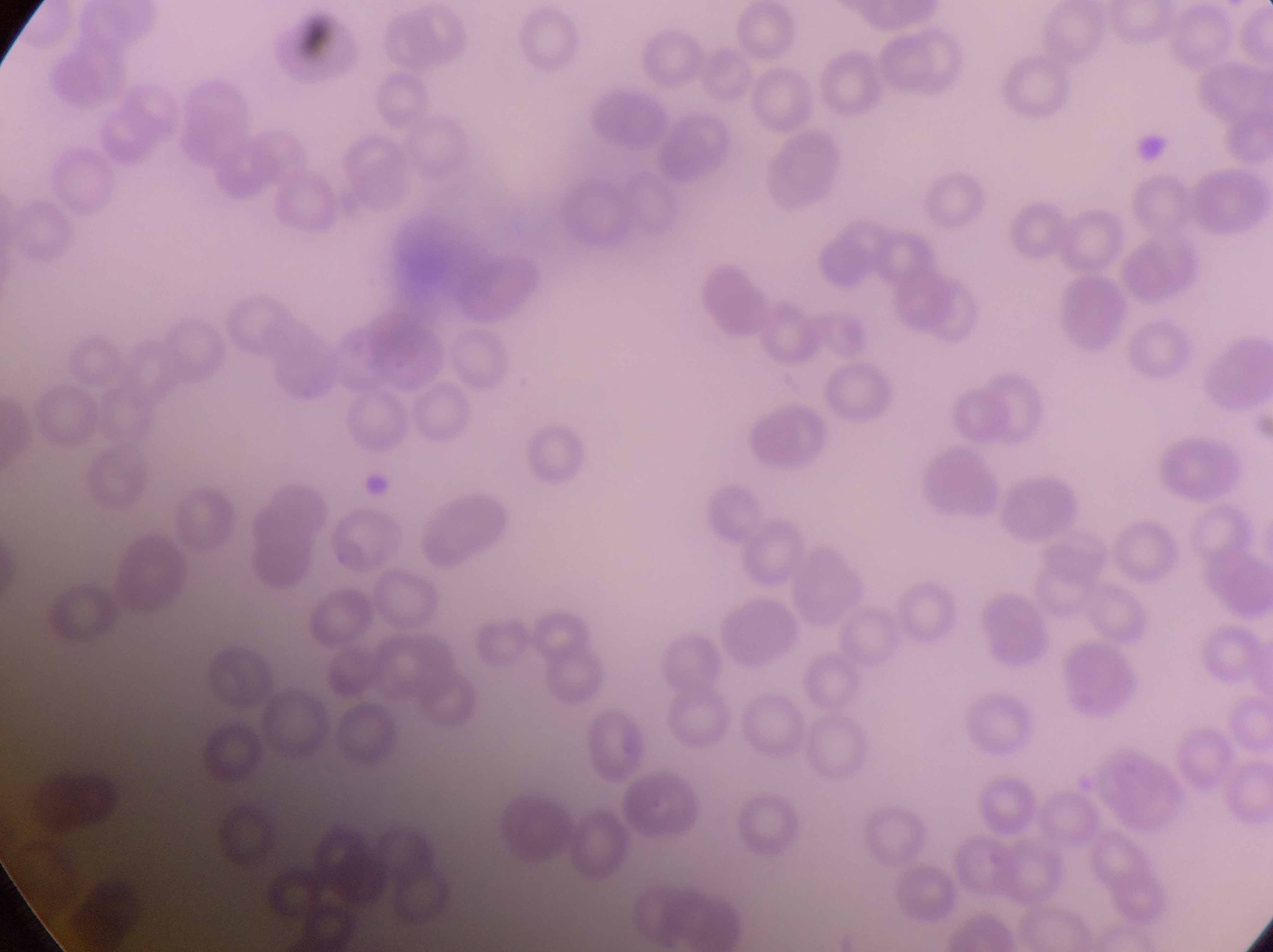
Approximate bounding boxes as left top right bottom in pixels.
Summary:
  - Artifact (platelet-like body, stain precipitate, or debris) locations: 1130 130 1170 169
  - Parasitised red blood cell locations: 325 509 413 579
  - Preparation: thin blood smear
  - Field of view: single
  - Magnification: 1000x
  - Country: Uganda
  - Capture: smartphone photograph through the eyepiece of an Olympus CX-23 microscope
  - Image size: 1273×952 pixels